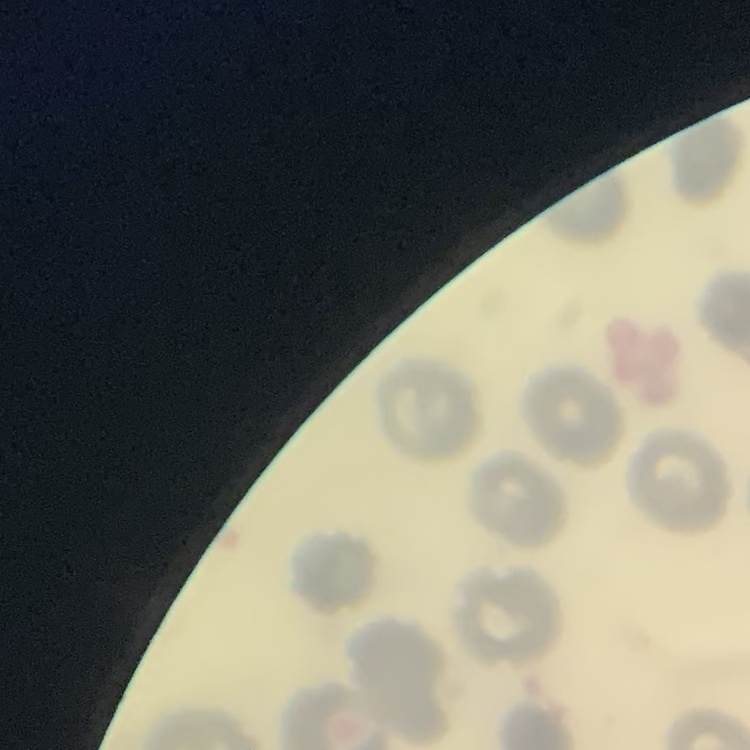
{
  "red_blood_cell_morphology": "no rouleaux formation",
  "preparation": "thin blood smear",
  "stain": "Field's or Giemsa",
  "image_type": "square crop of a larger photomicrograph"
}